Name the parasite shown.
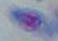

This is Toxoplasma gondii.

Micrograph. 1000x magnification.